Identify the cell.
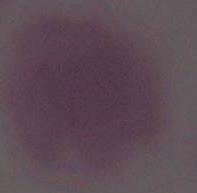
An erythrocyte.

1000x magnification. Photomicrograph.